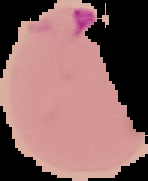
preparation: thin blood film
image_size: 148×181 pixels
result: Plasmodium parasites detected
image_type: segmented cell region with the area outside set to black